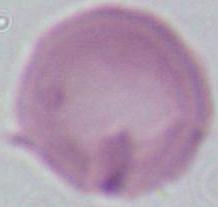
{
  "modality": "photomicrograph",
  "magnification": "1000x",
  "identification": "erythrocyte"
}